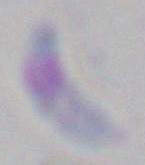

magnification: 1000x
identification: Toxoplasma gondii
modality: micrograph